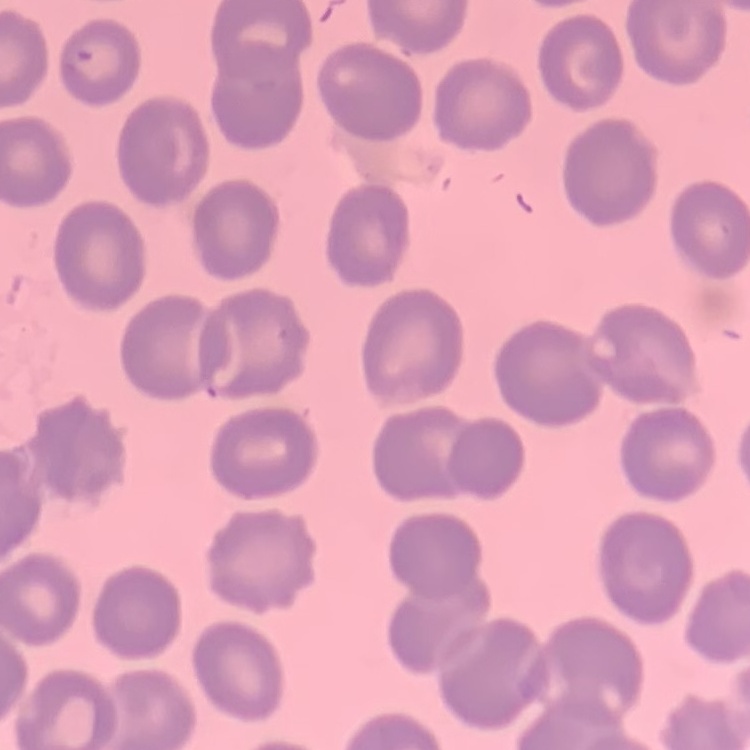
Summary:
  - Red blood cell morphology: no rouleaux formation
  - Image type: square crop of a larger photomicrograph
  - Stain: Field's or Giemsa
  - Preparation: thin blood film